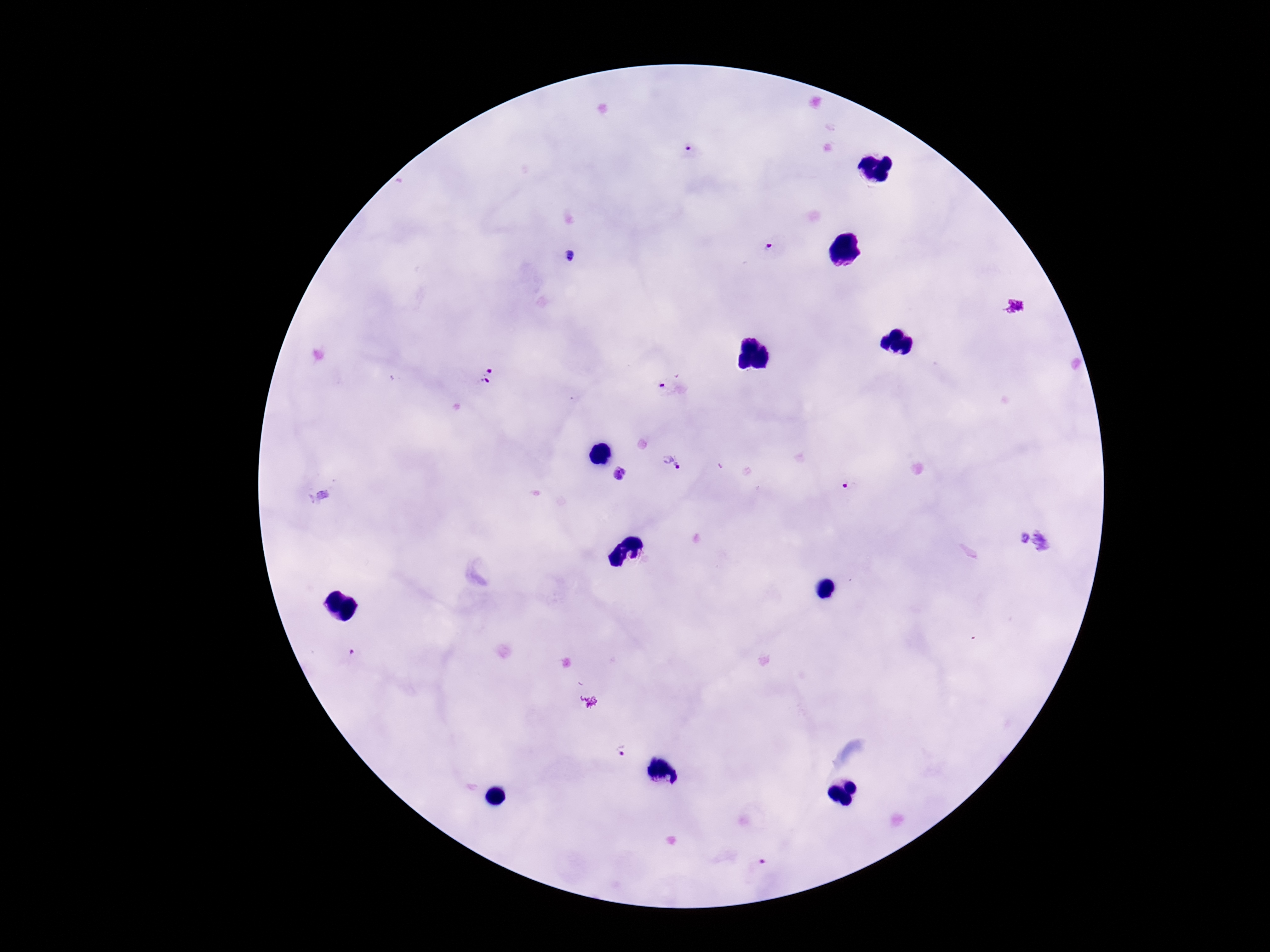
Approximate centers as (x, y) in pixels. Plasmodium parasite locations: (687, 153), (772, 248), (571, 254), (487, 374), (664, 386), (672, 461), (621, 474), (845, 488), (351, 655), (621, 750), (758, 864). Thick blood film. Photographed through the microscope eyepiece with a smartphone camera. Image is 1270×952 pixels. Patient malaria status: infected. Giemsa stain. 100x magnification. Single field of view.